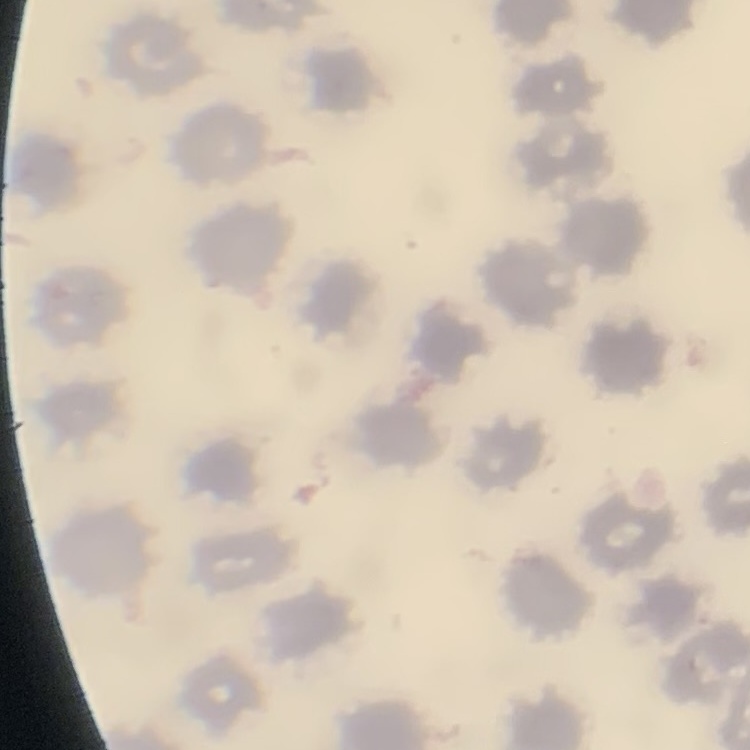

Summary:
  - Erythrocyte morphology: no rouleaux formation
  - Preparation: thin blood film
  - Stain: Field's or Giemsa
  - Image type: square crop of a larger photomicrograph